Classify this cell by malaria status.
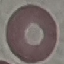
Uninfected.

Thin blood smear. Photographed with a smartphone camera at the microscope eyepiece. Cell patch, automatically extracted from a larger field of view and resized to 64 × 64 pixels. Giemsa stain.